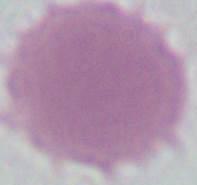

An erythrocyte is seen. Micrograph. Captured at 1000x magnification.